Assess this cell for malaria.
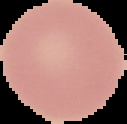
Uninfected.

From a thin blood film. Image is 127×124 pixels. Segmented cell region on a black background.